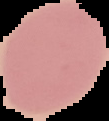 Segmented cell region on a black background. Malaria status: uninfected. From a thin blood film. Image is 109×121 pixels.